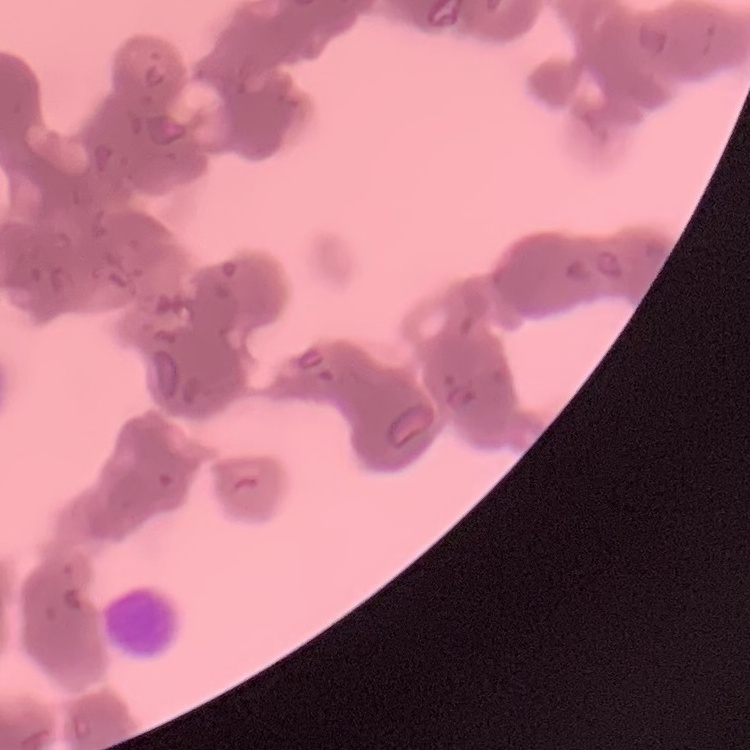

Summary:
  - Erythrocyte morphology: rouleaux formation
  - Image type: one tile cut from a larger photomicrograph
  - Stain: Field's or Giemsa
  - Preparation: thin blood film